Assess this cell for malaria.
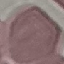

It is uninfected.

Summary:
  - Preparation: thin blood film
  - Image type: automatically extracted cell patch, resized to 64 × 64 pixels
  - Stain: Giemsa
  - Capture: smartphone camera at the microscope eyepiece